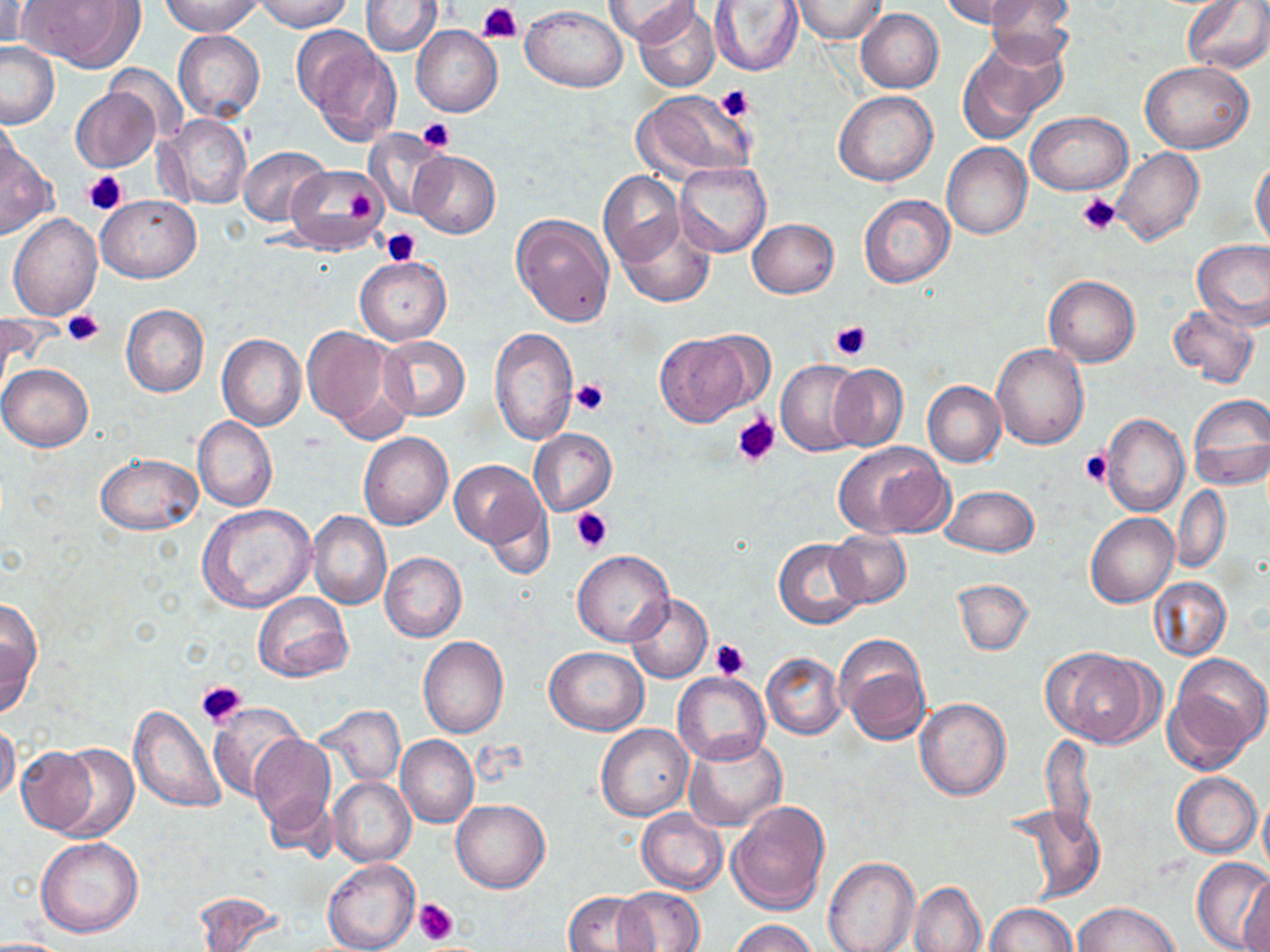
Summary:
  - Coordinate format: approximate bounding boxes as (x1, y1, x2, y2) in pixels
  - Platelet locations: (480, 4, 524, 43), (716, 84, 755, 122), (417, 118, 456, 153), (82, 170, 127, 214), (337, 183, 377, 226), (1077, 194, 1121, 237), (382, 229, 420, 266), (62, 307, 107, 346), (830, 320, 872, 361), (570, 378, 609, 418), (734, 414, 780, 467), (1081, 450, 1112, 487), (572, 508, 612, 552), (710, 640, 750, 681), (196, 678, 247, 728), (413, 898, 459, 945)
  - Uninfected red blood cell locations: (0, 0, 32, 52), (160, 0, 263, 36), (254, 0, 354, 32), (607, 0, 697, 46), (789, 0, 885, 44), (943, 0, 1039, 28), (982, 0, 1074, 71), (1182, 0, 1270, 74), (26, 1, 144, 72), (361, 1, 442, 55), (708, 1, 804, 76), (634, 2, 720, 93), (522, 5, 626, 92), (855, 9, 944, 93), (412, 25, 503, 117), (173, 30, 264, 121), (297, 30, 401, 144), (959, 39, 1064, 144), (0, 42, 59, 127), (1140, 60, 1254, 153), (105, 65, 188, 143), (71, 88, 159, 172), (632, 89, 756, 184), (833, 90, 937, 187), (156, 112, 252, 209), (1027, 112, 1131, 194), (1, 114, 24, 192), (363, 130, 450, 219), (942, 141, 1032, 239), (0, 144, 57, 238), (238, 146, 331, 226), (1111, 147, 1206, 245), (410, 151, 500, 238), (1250, 159, 1270, 251), (675, 162, 772, 257), (286, 164, 389, 253), (598, 172, 684, 266), (859, 194, 953, 287), (95, 195, 200, 282), (511, 213, 615, 328), (8, 214, 103, 319), (615, 216, 715, 308), (747, 218, 839, 298), (1193, 241, 1270, 332), (355, 256, 450, 344), (1044, 274, 1140, 367), (121, 304, 209, 398), (1167, 304, 1259, 389), (303, 326, 404, 437), (488, 327, 578, 444), (654, 332, 757, 425), (217, 334, 306, 432), (377, 336, 470, 419), (992, 342, 1089, 448), (775, 360, 866, 457), (0, 364, 92, 452), (826, 364, 907, 450), (923, 381, 1005, 467), (1187, 394, 1270, 490), (1101, 414, 1189, 516), (192, 417, 276, 511), (529, 428, 616, 516), (359, 432, 453, 530), (832, 440, 953, 539), (96, 454, 202, 535), (449, 461, 548, 552), (940, 484, 1039, 556), (478, 485, 553, 577), (1170, 487, 1231, 572), (198, 504, 316, 611), (307, 510, 391, 610), (1086, 513, 1178, 607), (825, 530, 910, 606), (774, 538, 868, 629), (572, 550, 675, 646), (380, 552, 466, 641), (1149, 577, 1231, 660), (953, 579, 1033, 655), (253, 592, 353, 681), (626, 594, 711, 683), (0, 600, 41, 716), (834, 635, 931, 745), (419, 636, 509, 738), (545, 646, 648, 735), (1043, 648, 1158, 747), (761, 653, 845, 739), (1168, 653, 1268, 766), (674, 672, 770, 765), (914, 699, 1011, 800), (207, 702, 305, 799), (314, 704, 405, 787), (128, 706, 226, 814), (0, 721, 20, 806), (595, 723, 693, 821), (247, 734, 335, 834), (1041, 734, 1096, 839), (684, 735, 788, 832), (396, 736, 478, 827), (43, 743, 139, 841), (14, 748, 103, 837), (1173, 773, 1261, 858), (329, 777, 416, 867), (263, 789, 338, 862), (1257, 795, 1270, 877), (452, 800, 550, 892), (728, 801, 830, 915), (1002, 803, 1105, 903), (637, 808, 729, 894), (35, 836, 143, 937), (824, 856, 919, 952), (324, 857, 419, 952), (1192, 857, 1270, 952), (1240, 874, 1270, 952), (909, 881, 987, 952), (614, 887, 705, 951), (563, 890, 655, 952), (191, 893, 289, 951), (1073, 902, 1179, 952), (985, 903, 1078, 952), (727, 919, 818, 952)
  - Slide-level diagnosis: no evidence of blood parasites
  - Modality: light microscopy
  - Preparation: thin blood film
  - Magnification: 1000x
  - Stain: May-Grünwald-Giemsa
  - Image size: 1270×952 pixels
  - Field of view: one of a larger specimen